Classify this cell by malaria status.
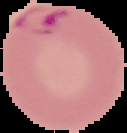
It is parasitized.

Image is 127×133 pixels. Segmented cell region on a black background. From a thin blood smear.